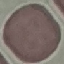

Malaria status: uninfected. Giemsa-stained preparation. Acquired by smartphone through the microscope eyepiece. Automatically extracted cell patch, resized to 64 × 64 pixels. Thin blood film.